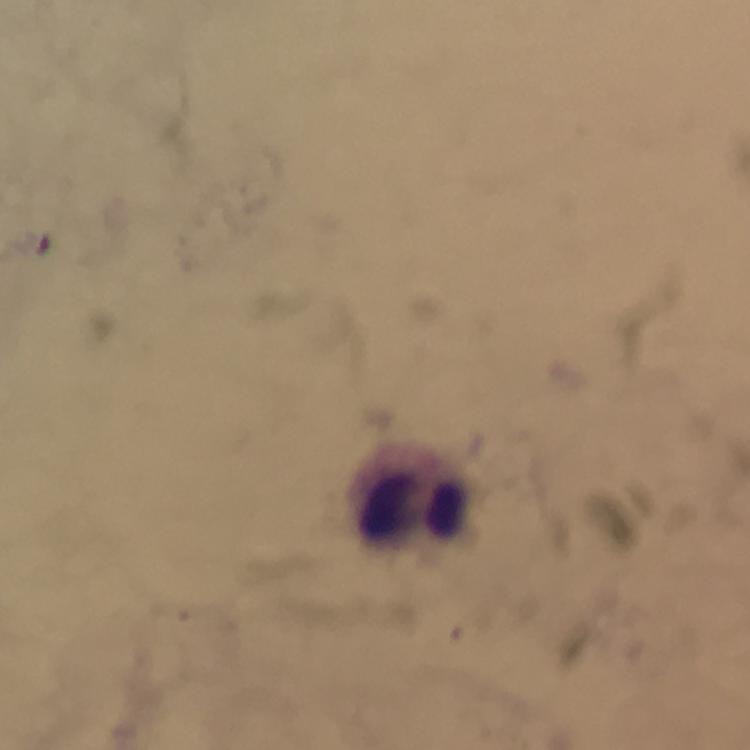

magnification = 100x
malaria parasites = none detected
image size = 750×750 pixels
preparation = thick blood smear
immersion oil = applied
cropped from = a single field of view
context = from a diagnostic examination for malaria
capture = smartphone mounted on the microscope
stain = Giemsa
leukocyte locations = approximate centers as [x, y] in pixels: [417, 496]